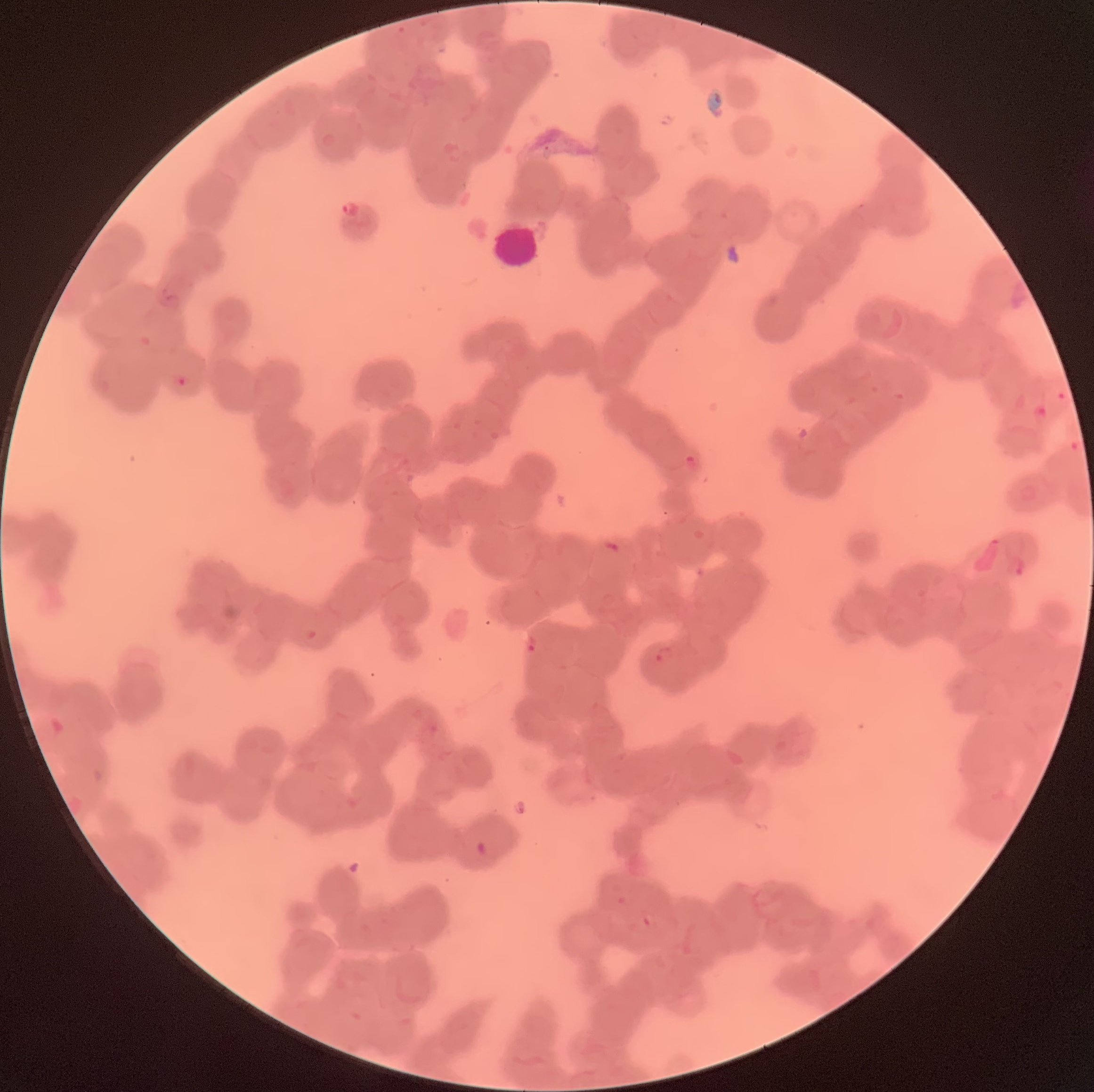

Approximate bounding boxes as named x1/y1/x2/y2 corners in pixels. Plasmodium parasite locations: (x1=340, y1=200, x2=366, y2=221), (x1=163, y1=287, x2=175, y2=304), (x1=174, y1=375, x2=194, y2=387), (x1=684, y1=454, x2=700, y2=469), (x1=1008, y1=556, x2=1026, y2=578), (x1=525, y1=634, x2=537, y2=654), (x1=656, y1=645, x2=677, y2=666). White blood cell locations: (x1=491, y1=225, x2=543, y2=269). Light microscopy. Image is 1094×1092 pixels. The red blood cells show rouleaux formation. Thin blood smear.